Assess the morphology of the erythrocytes.
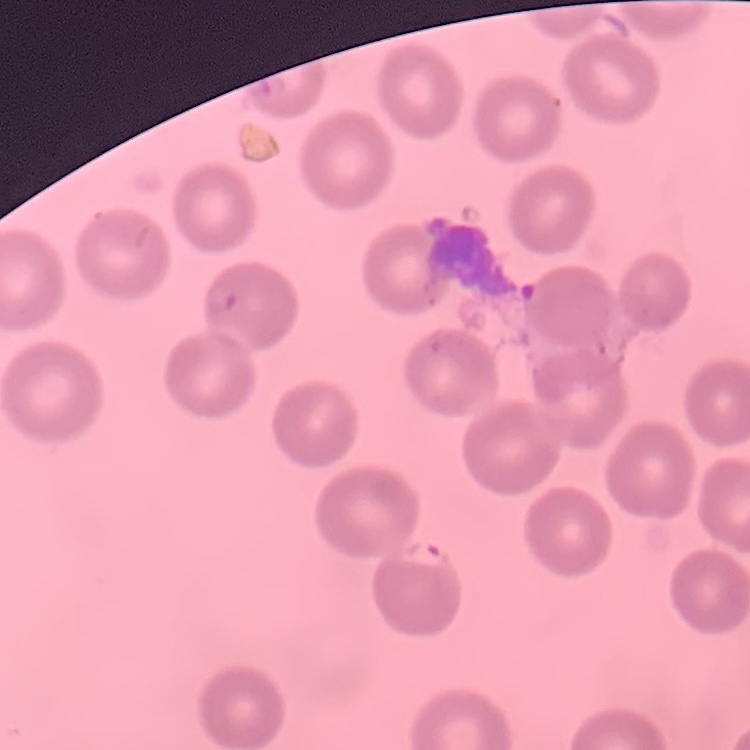
They show no rouleaux formation.

Thin peripheral smear. One tile cut from a larger photomicrograph. Field's or Giemsa stain.